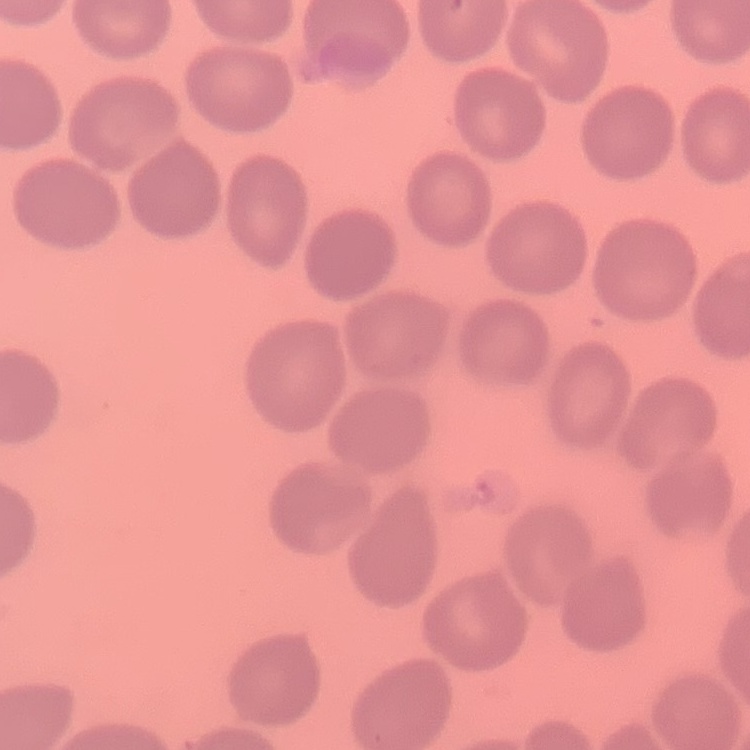

Summary:
  - Erythrocyte morphology: no rouleaux formation
  - Preparation: thin blood smear
  - Image type: one tile cut from a larger photomicrograph
  - Stain: Field's or Giemsa